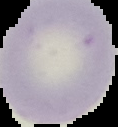

malaria status = uninfected
preparation = thin blood smear
image size = 118×127 pixels
image type = cell region segmented out of the field of view; surrounding area masked to black